Assess this cell for malaria.
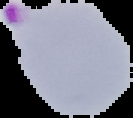
It is parasitized.

Summary:
  - Preparation: thin blood film
  - Image size: 133×118 pixels
  - Image type: segmented cell region on a black background